Report the malaria status of this cell.
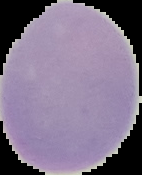

Uninfected.

Summary:
  - Preparation: thin blood smear
  - Image type: cell region segmented out of the field of view; surrounding area masked to black
  - Image size: 142×175 pixels